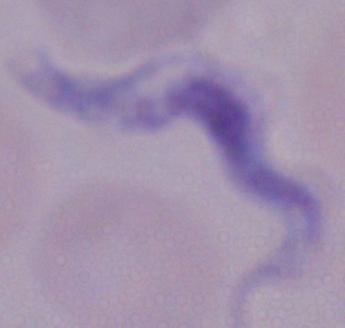

{
  "modality": "photomicrograph",
  "identification": "trypanosome",
  "magnification": "1000x"
}